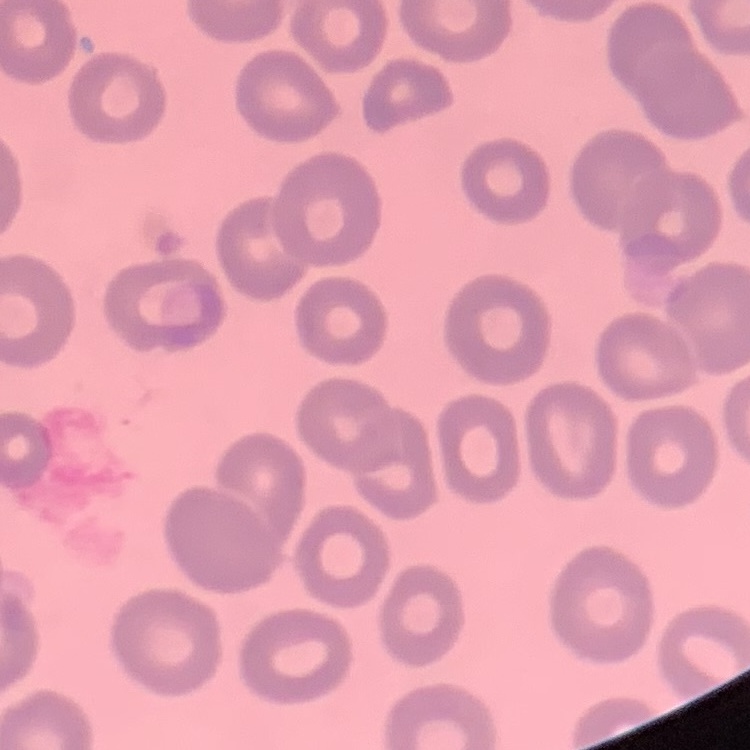 The erythrocytes show no rouleaux formation. Thin blood film. One tile cut from a larger photomicrograph. Field's or Giemsa stain.